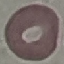
Summary:
  - Result: no malaria parasites detected
  - Image type: automatically extracted cell patch, resized to 64 × 64 pixels
  - Preparation: thin blood smear
  - Capture: smartphone through the microscope eyepiece
  - Stain: Giemsa